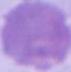

Micrograph. Captured at 1000x magnification. A red blood cell is seen.